Report the malaria status of this cell.
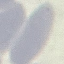
Uninfected.

Giemsa-stained preparation. Thin blood film. Automatically extracted cell patch, resized to 64 × 64 pixels. Photographed with a smartphone camera at the microscope eyepiece.